Describe the morphology of the red blood cells.
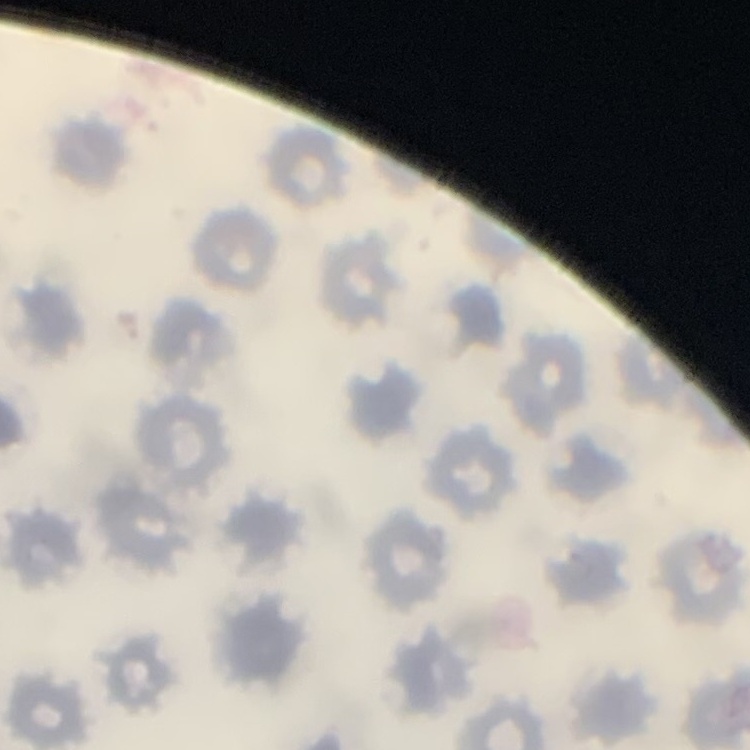

No rouleaux formation.

Summary:
  - Image type: one tile cut from a larger photomicrograph
  - Stain: Field's or Giemsa
  - Preparation: thin blood film